Assess this cell for malaria.
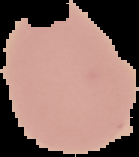
It is uninfected.

From a thin blood film. Segmented cell region on a black background. Image is 139×157 pixels.